Rate the background quality.
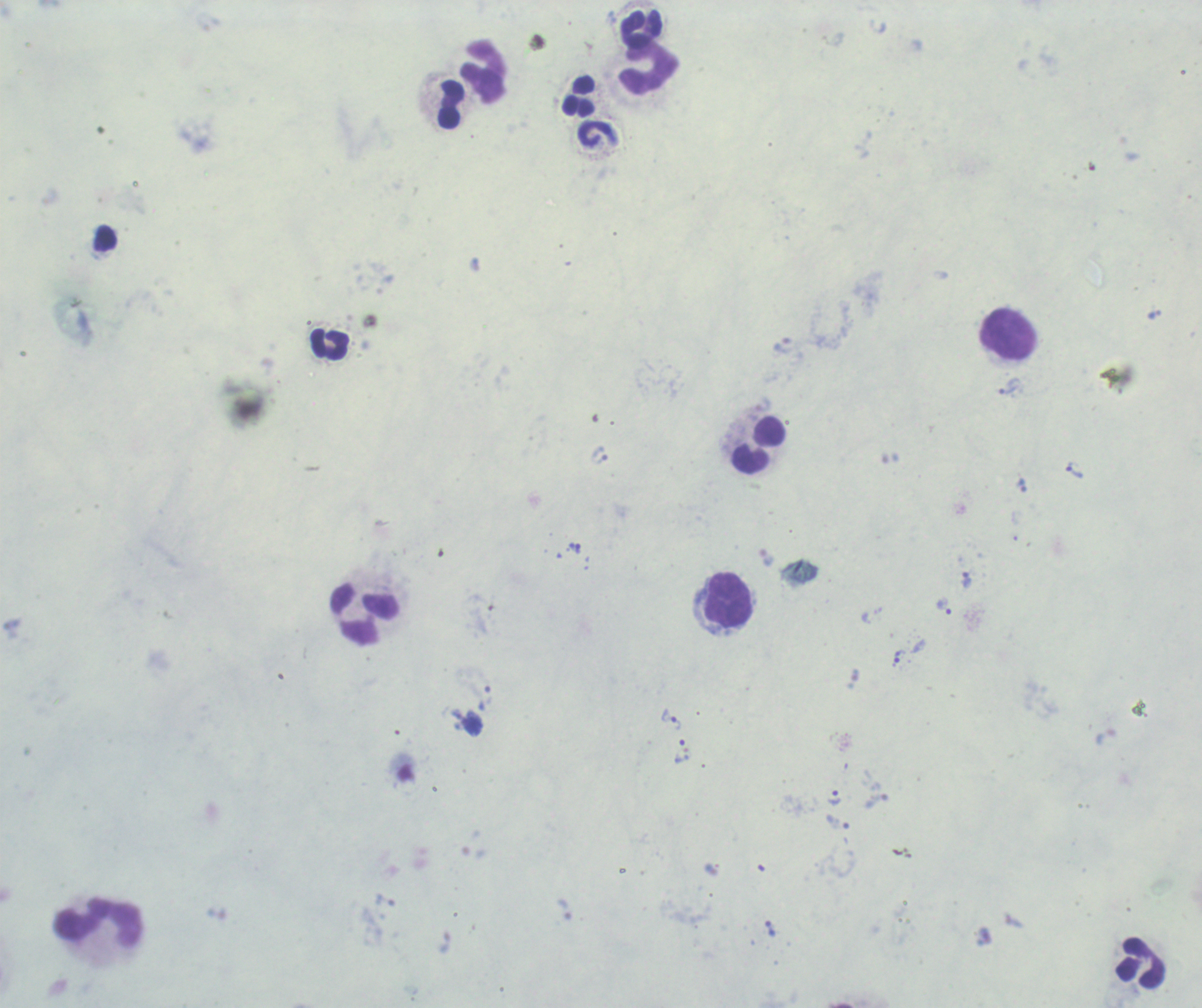
Unsatisfactory.

Approximate object centers, in pixels from the top-left corner. Leukocyte locations: (x=641, y=28), (x=649, y=69), (x=484, y=71), (x=580, y=97), (x=448, y=104), (x=1007, y=335), (x=329, y=344), (x=759, y=446), (x=728, y=599), (x=364, y=614), (x=98, y=923), (x=1139, y=962). Trophozoite locations: (x=783, y=345), (x=1008, y=390), (x=763, y=405), (x=1074, y=470), (x=967, y=580), (x=945, y=606), (x=900, y=656), (x=671, y=718), (x=834, y=797), (x=770, y=929). Image is 1202×1008 pixels. Previously used in a real diagnosis. One field from this slide. Captured at 100x magnification. Result: Plasmodium parasites detected. Romanowsky stain. Thick blood smear.